Report the malaria status of this cell.
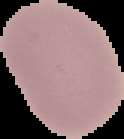
It is uninfected.

Image is 124×139 pixels. From a thin blood film. Segmented cell region on a black background.